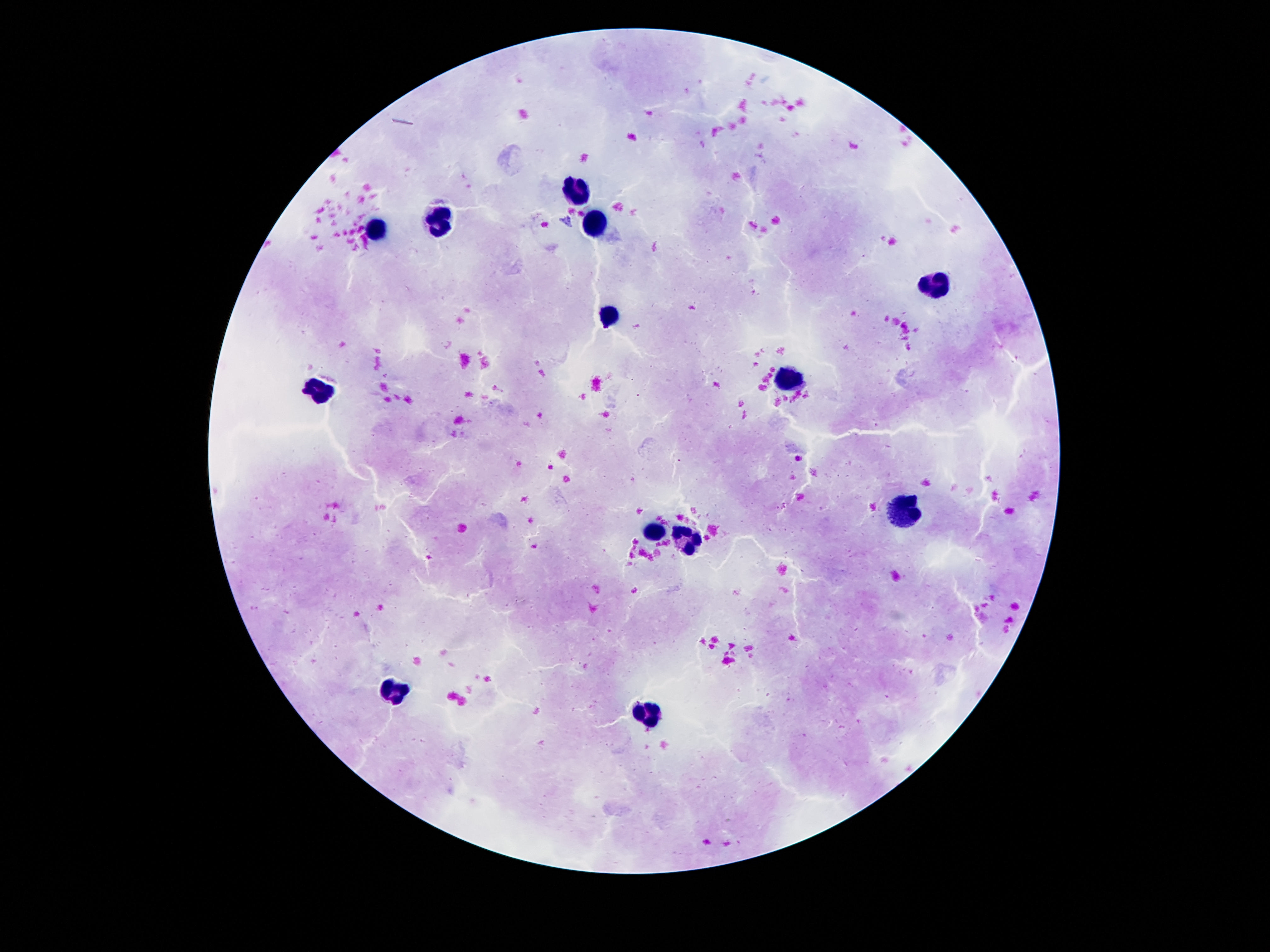
Approximate centers as [x, y] in pixels.
Summary:
  - Leukocyte locations: [583, 192], [442, 222], [598, 224], [378, 231], [934, 285], [606, 320], [793, 379], [319, 390], [900, 508], [655, 533], [687, 538], [393, 688], [643, 718]
  - Preparation: thick blood smear
  - Patient malaria status: negative
  - Magnification: 100x
  - Capture: smartphone camera through the microscope eyepiece
  - Field of view: single
  - Image size: 1270×952 pixels
  - Stain: Giemsa